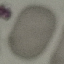
malaria status = uninfected
preparation = thin blood film
image type = automatically extracted cell patch, resized to 64 × 64 pixels
capture = smartphone camera at the microscope eyepiece
stain = Giemsa